Name the parasite shown.
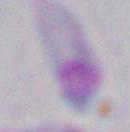

Toxoplasma gondii.

{
  "modality": "photomicrograph",
  "magnification": "1000x"
}